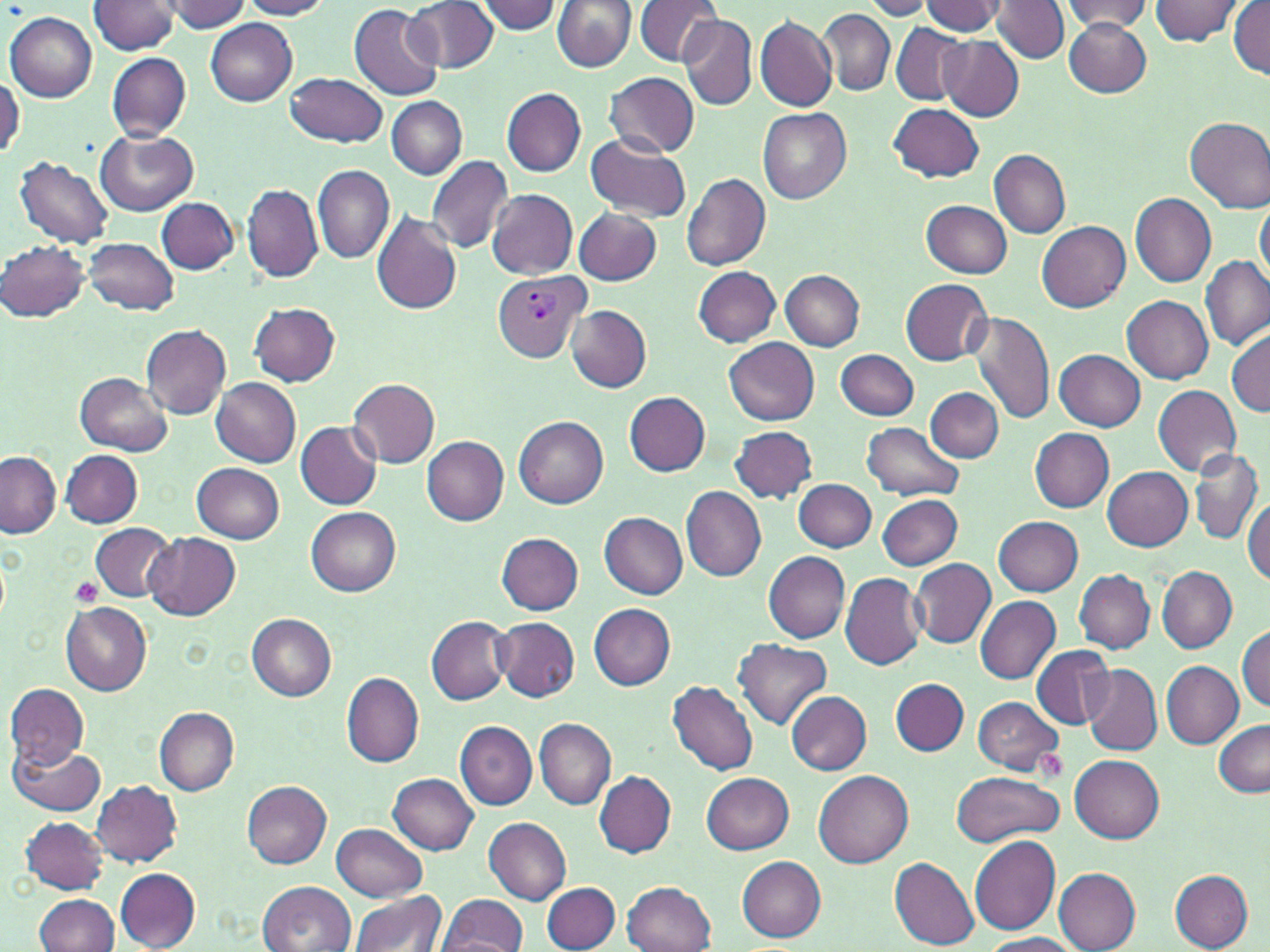
slide_level_diagnosis: Plasmodium vivax
modality: optical microscopy
uninfected_red_blood_cell_locations: 'approximate bounding boxes as (x1,y1)-(x2,y2) corner pairs in pixels: (160,0)-(250,33), (406,0)-(498,73), (475,0)-(562,34), (552,0)-(636,72), (634,0)-(721,66), (860,0)-(935,20), (1061,0)-(1152,32), (1149,0)-(1244,47), (89,1)-(178,53), (240,1)-(332,20), (919,1)-(1007,35), (992,1)-(1068,63), (1230,1)-(1269,81), (349,4)-(445,101), (818,9)-(893,95), (7,12)-(97,102), (680,14)-(756,111), (756,14)-(837,112), (205,18)-(297,104), (1064,20)-(1150,97), (891,24)-(968,104), (939,35)-(1023,120), (107,52)-(191,141), (286,72)-(386,147), (605,72)-(699,157), (1,74)-(23,159), (501,88)-(586,176), (386,97)-(467,179), (888,103)-(984,182), (757,107)-(851,203), (1185,117)-(1270,212), (97,127)-(199,214), (585,133)-(691,223), (988,148)-(1070,238), (426,154)-(514,253), (13,156)-(115,249), (313,164)-(395,263), (681,172)-(770,271), (243,183)-(322,283), (486,188)-(577,279), (1130,193)-(1217,289), (1255,195)-(1269,287), (156,196)-(239,274), (921,200)-(1012,278), (573,207)-(661,284), (370,213)-(463,315), (1037,220)-(1131,310), (84,237)-(179,316), (1,242)-(89,321), (1201,256)-(1269,350), (692,265)-(781,348), (780,270)-(865,350), (900,278)-(993,366), (1122,296)-(1213,384), (250,303)-(341,386), (566,306)-(652,391), (969,311)-(1056,425), (140,324)-(231,419), (1228,327)-(1270,416), (724,338)-(819,425), (837,348)-(919,421), (1055,350)-(1145,430), (75,373)-(172,454), (211,378)-(302,467), (347,378)-(439,468), (1153,385)-(1241,475), (925,387)-(1003,462), (624,391)-(710,477), (514,416)-(607,508), (295,422)-(383,510), (862,422)-(964,502), (729,425)-(818,503), (1031,428)-(1114,512), (422,437)-(509,524), (1189,448)-(1263,544), (61,449)-(143,527), (0,452)-(62,538), (192,463)-(286,543), (1102,467)-(1193,550), (794,478)-(877,552), (682,487)-(766,581), (876,495)-(961,569), (1244,498)-(1269,587), (306,507)-(400,596), (598,511)-(686,599), (994,516)-(1082,595), (90,522)-(177,603), (143,532)-(240,621), (497,534)-(584,614), (762,551)-(850,643), (911,560)-(995,648), (1157,566)-(1236,652), (1074,569)-(1154,652), (841,573)-(928,671), (975,596)-(1061,685), (60,601)-(151,695), (588,604)-(675,690), (246,614)-(337,701), (492,615)-(580,702), (426,617)-(511,705), (1236,626)-(1269,712), (733,638)-(832,729), (1031,645)-(1114,728), (1161,660)-(1244,747), (1082,663)-(1161,753), (342,673)-(425,768), (891,678)-(969,756), (666,680)-(758,776), (5,683)-(88,766), (786,692)-(872,774), (972,697)-(1064,774), (154,707)-(240,796), (535,717)-(615,810), (1212,719)-(1270,797), (455,721)-(537,810), (8,741)-(105,816), (1071,756)-(1163,842), (813,769)-(913,868), (951,769)-(1066,846), (594,770)-(676,856), (389,772)-(478,855), (702,773)-(794,855), (91,780)-(182,866), (241,781)-(332,868), (19,816)-(109,893), (484,818)-(571,904), (330,822)-(427,900), (969,836)-(1060,935), (739,856)-(825,941), (889,856)-(980,949), (115,868)-(201,950), (1053,868)-(1140,952), (1169,869)-(1254,951), (258,881)-(356,952), (624,881)-(717,952), (542,882)-(621,951), (349,892)-(446,952), (34,894)-(118,952), (439,894)-(529,952), (977,933)-(1081,952)'
plasmodium_vivax_infected_red_blood_cell_locations: 'approximate bounding boxes as (x1,y1)-(x2,y2) corner pairs in pixels: (493,270)-(589,361)'
preparation: thin blood film
magnification: 1000x
platelet_locations: 'approximate bounding boxes as (x1,y1)-(x2,y2) corner pairs in pixels: (70,576)-(105,607), (1034,749)-(1068,783)'
image_size: 1270×952 pixels
field_of_view: single
stain: May-Grünwald-Giemsa